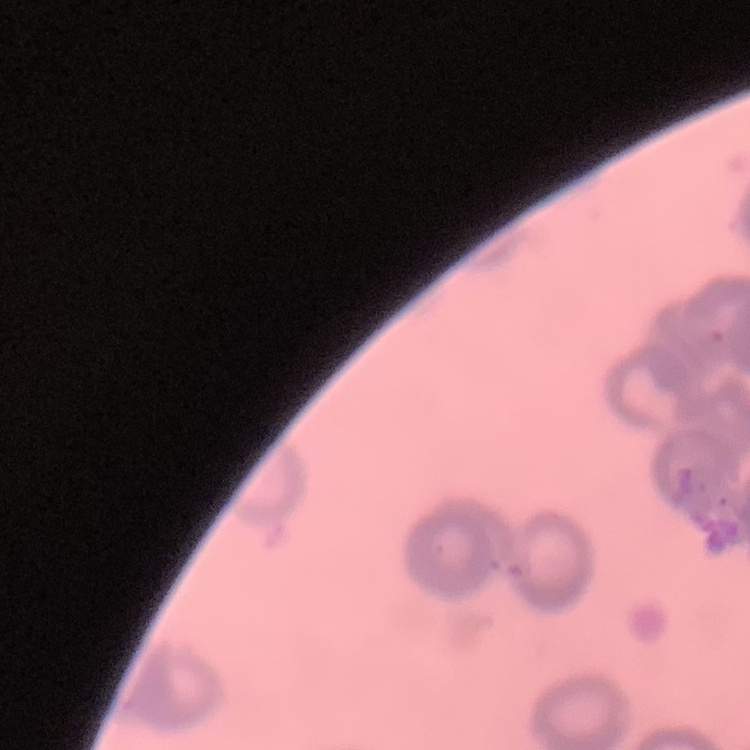

The erythrocytes exhibit rouleaux formation. Stained with either Field's or Giemsa. Thin blood film. Square crop of a larger photomicrograph.